State which cell type is depicted.
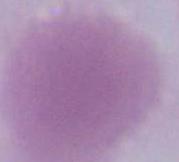

An erythrocyte.

Micrograph. Captured at 1000x magnification.